Give the position of every Plasmodium parasite, noting whether each is a trophozoite, schizont, or gametocyte.
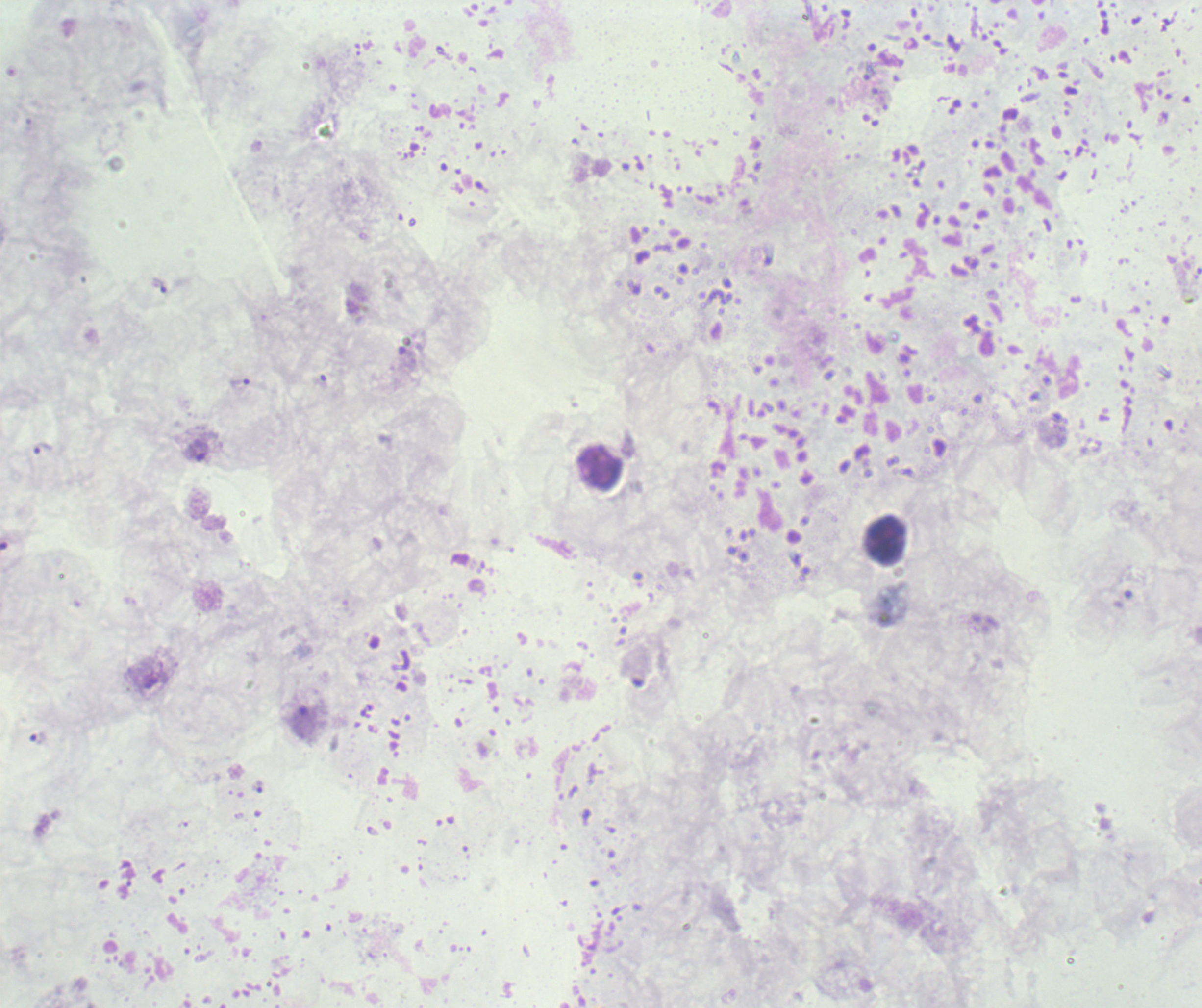
Approximate centers as {x, y} in pixels.
Trophozoites: {158, 285}, {239, 385}, {43, 448}, {197, 451}, {38, 738}.
No schizont or gametocyte forms observed.

Approximate centers as {x, y} in pixels.
Summary:
  - Leukocyte locations: {602, 469}
  - Stain: Romanowsky
  - Preparation: thick blood film
  - Magnification: 100x
  - Context: previously used in a real diagnosis
  - Image size: 1202×1008 pixels
  - Field of view: single
  - Background quality: unsatisfactory